Describe the morphology of the red blood cells.
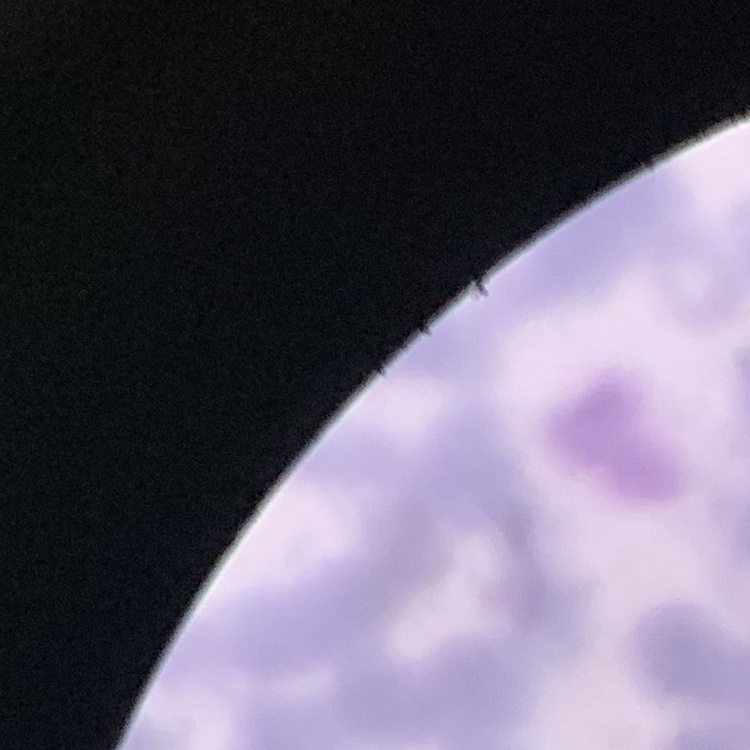
Rouleaux formation.

One tile cut from a larger photomicrograph. Stained with either Field's or Giemsa. Thin blood film.